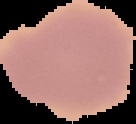
image type = segmented cell region on a black background
preparation = thin blood smear
malaria status = uninfected
image size = 136×124 pixels